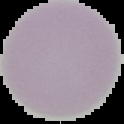

The area outside the segmented cell region is set to black. From a thin blood smear. Image is 124×124 pixels. Result: no malaria parasites seen.